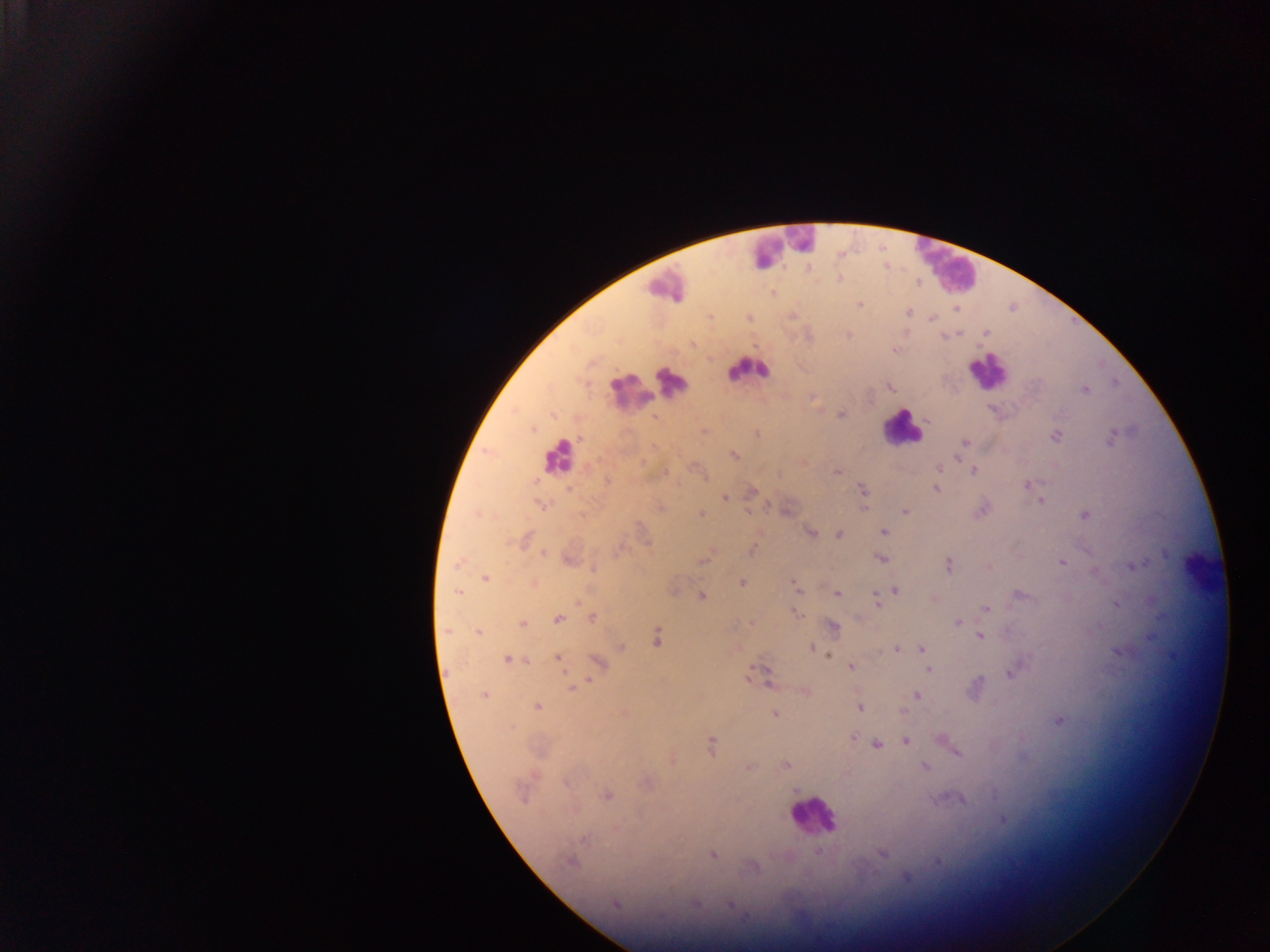

leukocyte locations = approximate centers as [x, y] in pixels: [784, 246], [949, 268], [664, 287], [748, 370], [987, 371], [673, 383], [629, 392], [901, 427], [559, 455], [1199, 571], [812, 815]
Plasmodium parasite locations = approximate centers as [x, y] in pixels: [839, 279], [916, 281], [860, 304], [908, 312], [792, 315], [749, 318], [931, 318], [986, 333], [692, 344], [894, 350], [890, 387], [1085, 389], [841, 414], [654, 417], [703, 431], [756, 433], [1057, 435], [964, 443], [733, 455], [939, 469], [973, 470], [837, 472], [607, 481], [1028, 484], [936, 489], [862, 490], [750, 491], [724, 497], [1041, 500], [539, 504], [659, 507], [864, 507], [748, 510], [905, 511], [701, 513], [1084, 515], [884, 532], [810, 533], [839, 534], [522, 541], [751, 549], [709, 550], [542, 552], [705, 557], [569, 559], [881, 559], [459, 562], [1062, 562], [948, 565], [1135, 565], [988, 566], [592, 568], [1095, 570], [486, 578], [741, 582], [532, 583], [795, 587], [893, 589], [457, 591], [837, 593], [1020, 594], [701, 596], [932, 598], [875, 602], [1116, 604], [985, 609], [796, 612], [591, 618], [558, 619], [958, 621], [751, 622], [522, 623], [832, 627], [478, 631], [980, 637], [657, 638], [621, 648], [812, 648], [895, 648], [921, 648], [557, 658], [508, 660], [598, 663], [851, 666], [928, 670], [1012, 673], [762, 674], [768, 681], [573, 687], [976, 688], [805, 692], [916, 694], [484, 696], [537, 706], [859, 708], [624, 713], [775, 714], [1059, 719], [852, 737], [906, 740], [871, 741], [711, 745], [876, 745], [950, 746], [956, 750], [671, 758], [786, 764], [748, 767], [924, 767], [647, 782], [605, 796], [960, 799], [1002, 819], [881, 853], [712, 854], [571, 861], [753, 866], [907, 877], [616, 904], [697, 904], [732, 905]
country = Ghana
preparation = thick blood film
field of view = single
capture = mobile-phone photograph through a microscope
image size = 1270×952 pixels